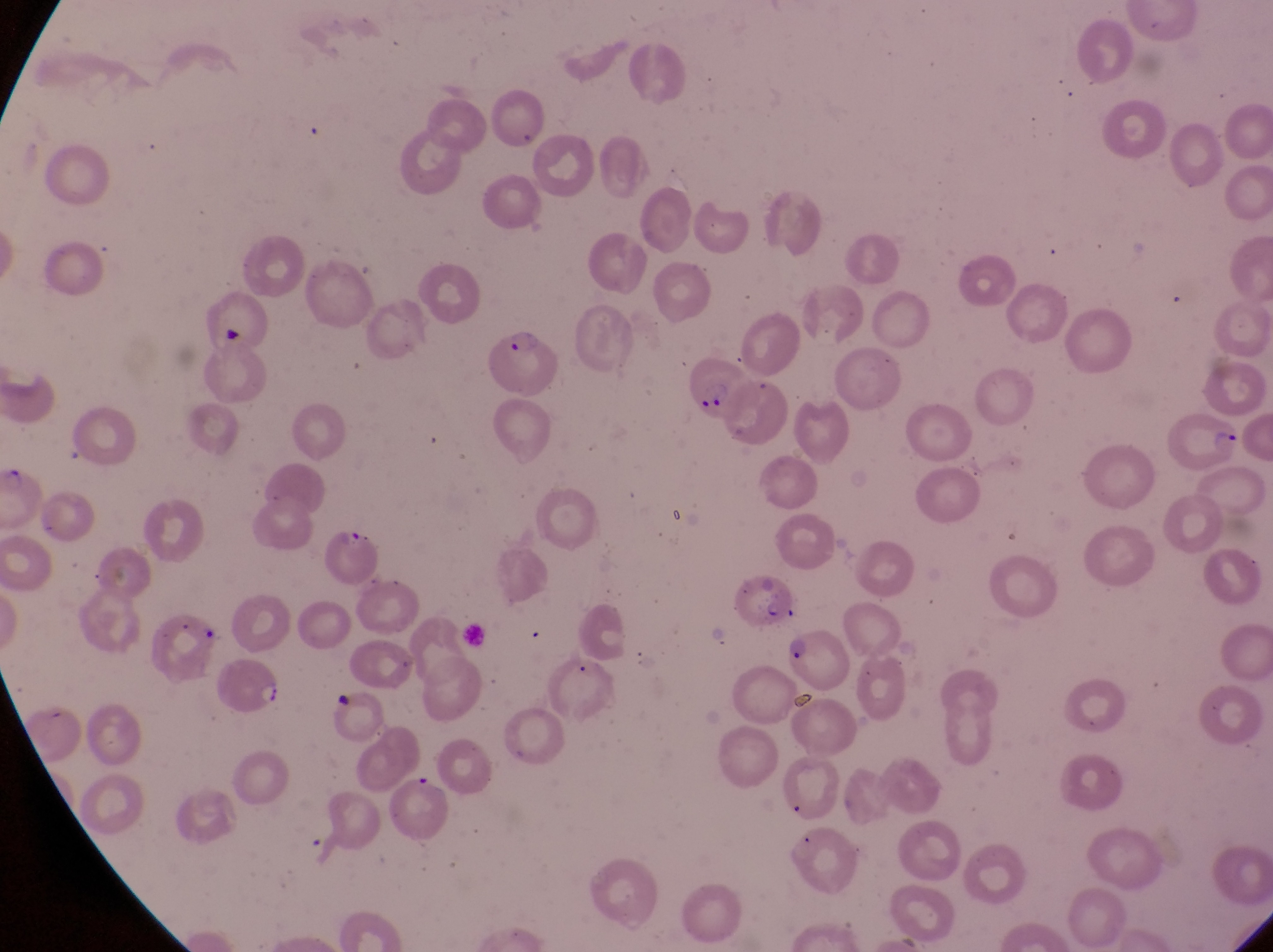

Approximate bounding boxes as [left, top, right, bottom] in pixels. Parasitised red blood cell locations: [487, 320, 559, 398], [674, 350, 754, 427], [1165, 405, 1243, 473], [314, 519, 386, 589], [729, 572, 799, 632], [779, 624, 849, 691], [212, 659, 289, 716]. Captured by a smartphone held over the eyepiece of an Olympus CX-23 microscope. One field of view. At a magnification of 1000x. Collected in Uganda. Image is 1273×952 pixels. Thin blood film.